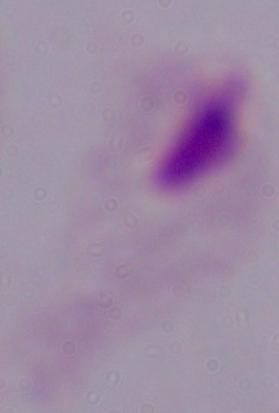
Summary:
  - Magnification: 1000x
  - Identification: trichomonad
  - Modality: micrograph